Assess the morphology of the red blood cells.
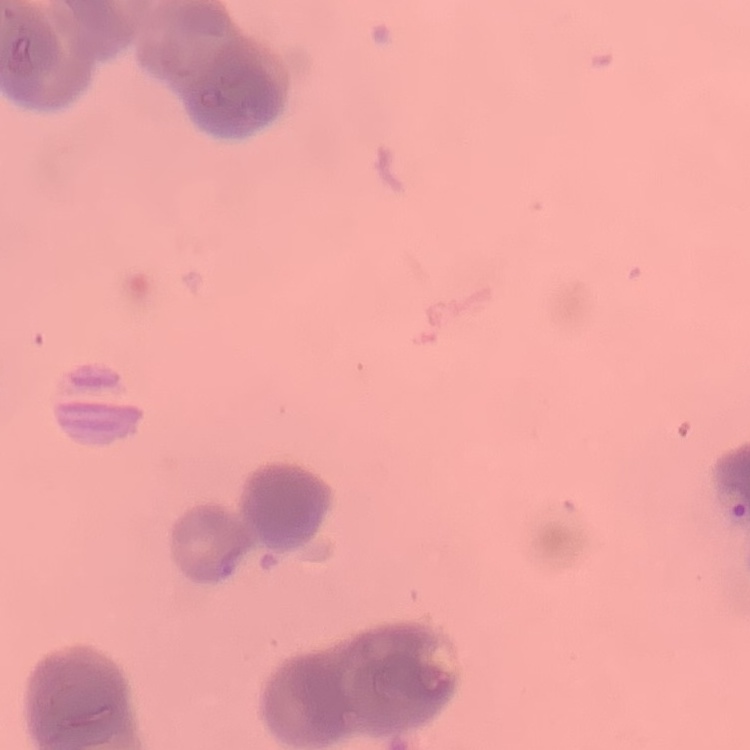

They show rouleaux formation.

Stained with either Field's or Giemsa. Thin peripheral smear. One tile cut from a larger photomicrograph.